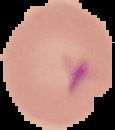

From a thin blood film. Result: Plasmodium parasites detected. Segmented cell region on a black background. Image is 115×130 pixels.